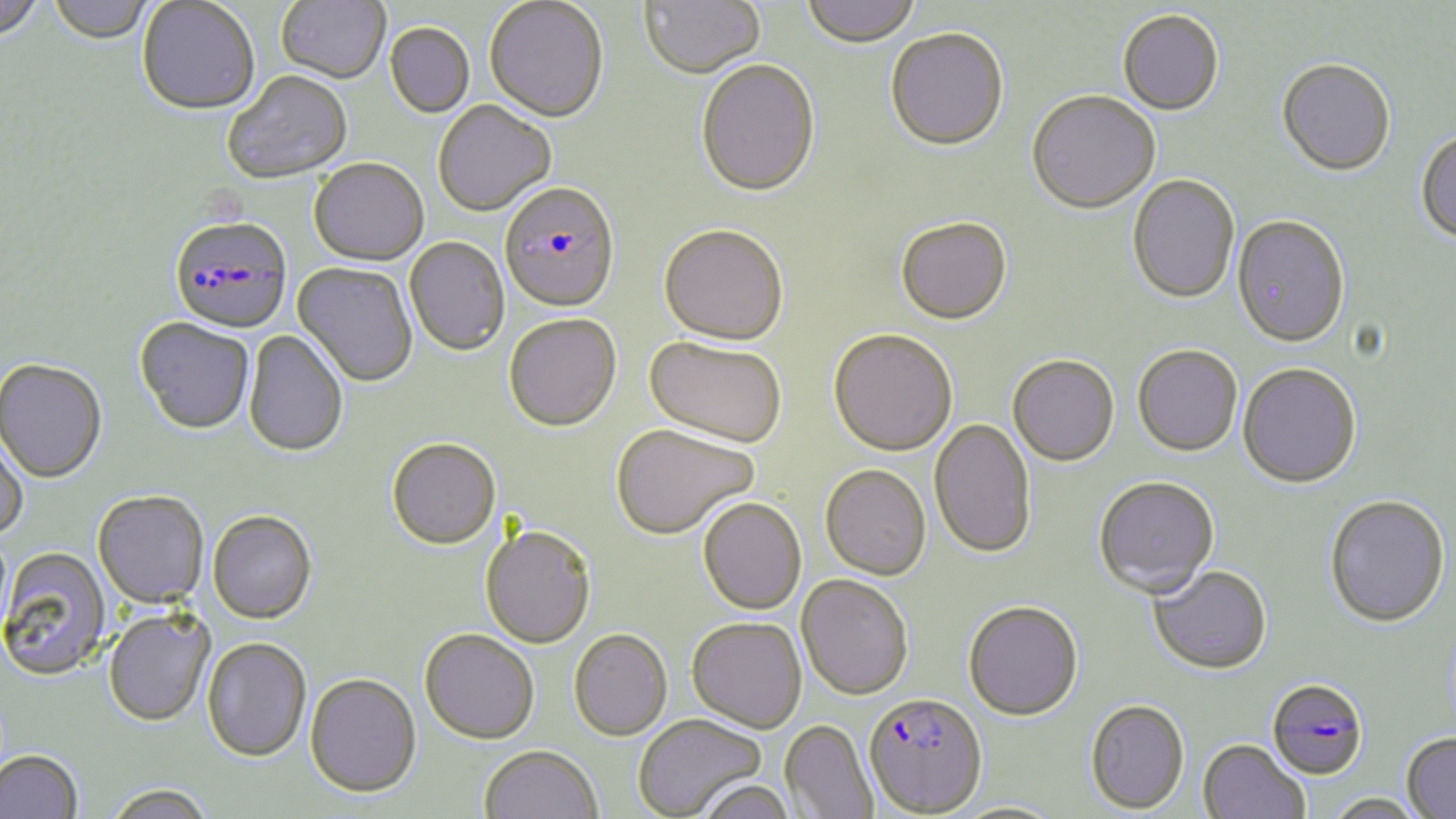
Approximate bounding boxes as named x1/y1/x2/y2 corners in pixels. Plasmodium falciparum-infected red blood cell locations: (x1=499, y1=184, x2=620, y2=314), (x1=169, y1=218, x2=292, y2=335), (x1=1266, y1=676, x2=1369, y2=780), (x1=863, y1=692, x2=987, y2=816). Uninfected red blood cell locations: (x1=0, y1=0, x2=46, y2=44), (x1=276, y1=0, x2=391, y2=86), (x1=484, y1=0, x2=608, y2=124), (x1=638, y1=0, x2=766, y2=80), (x1=800, y1=0, x2=922, y2=48), (x1=47, y1=1, x2=156, y2=47), (x1=137, y1=1, x2=259, y2=117), (x1=1117, y1=10, x2=1224, y2=116), (x1=385, y1=24, x2=475, y2=119), (x1=885, y1=28, x2=1009, y2=153), (x1=1276, y1=59, x2=1395, y2=175), (x1=696, y1=61, x2=821, y2=199), (x1=222, y1=73, x2=352, y2=186), (x1=1027, y1=91, x2=1161, y2=215), (x1=433, y1=101, x2=556, y2=217), (x1=1415, y1=129, x2=1456, y2=244), (x1=308, y1=159, x2=429, y2=267), (x1=1127, y1=174, x2=1240, y2=305), (x1=1232, y1=216, x2=1351, y2=348), (x1=896, y1=217, x2=1012, y2=325), (x1=659, y1=225, x2=788, y2=347), (x1=405, y1=237, x2=509, y2=357), (x1=292, y1=262, x2=418, y2=388), (x1=503, y1=314, x2=621, y2=432), (x1=134, y1=318, x2=255, y2=437), (x1=828, y1=328, x2=958, y2=456), (x1=244, y1=330, x2=349, y2=458), (x1=645, y1=337, x2=787, y2=448), (x1=1133, y1=345, x2=1242, y2=457), (x1=1007, y1=354, x2=1119, y2=467), (x1=0, y1=360, x2=107, y2=484), (x1=1238, y1=363, x2=1361, y2=489), (x1=929, y1=418, x2=1036, y2=559), (x1=610, y1=424, x2=759, y2=540), (x1=0, y1=427, x2=28, y2=541), (x1=386, y1=438, x2=501, y2=550), (x1=820, y1=464, x2=931, y2=580), (x1=1093, y1=476, x2=1220, y2=597), (x1=92, y1=491, x2=208, y2=608), (x1=1324, y1=495, x2=1450, y2=627), (x1=698, y1=497, x2=806, y2=615), (x1=207, y1=511, x2=317, y2=625), (x1=480, y1=525, x2=596, y2=649), (x1=0, y1=547, x2=110, y2=681), (x1=1147, y1=565, x2=1272, y2=674), (x1=796, y1=574, x2=914, y2=700), (x1=963, y1=599, x2=1083, y2=721), (x1=103, y1=609, x2=215, y2=728), (x1=687, y1=617, x2=806, y2=733), (x1=419, y1=629, x2=539, y2=745), (x1=569, y1=629, x2=672, y2=741), (x1=202, y1=638, x2=311, y2=763), (x1=305, y1=673, x2=422, y2=799), (x1=1084, y1=699, x2=1189, y2=814), (x1=633, y1=713, x2=766, y2=819), (x1=780, y1=719, x2=878, y2=818), (x1=1401, y1=732, x2=1456, y2=819), (x1=1198, y1=740, x2=1310, y2=819), (x1=479, y1=745, x2=602, y2=819), (x1=0, y1=750, x2=83, y2=819), (x1=694, y1=777, x2=795, y2=819), (x1=104, y1=785, x2=214, y2=819), (x1=1322, y1=793, x2=1429, y2=819). Slide-level diagnosis: Plasmodium falciparum. Image is 1456×819 pixels. One field of a larger specimen. Light microscopy. Thin blood smear. May-Grünwald-Giemsa-stained preparation. 1000x magnification.